Assess this cell for malaria.
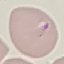

It is parasitized.

image type = automatically extracted cell patch, resized to 64 × 64 pixels
preparation = thin blood smear
stain = Giemsa
capture = smartphone camera at the microscope eyepiece